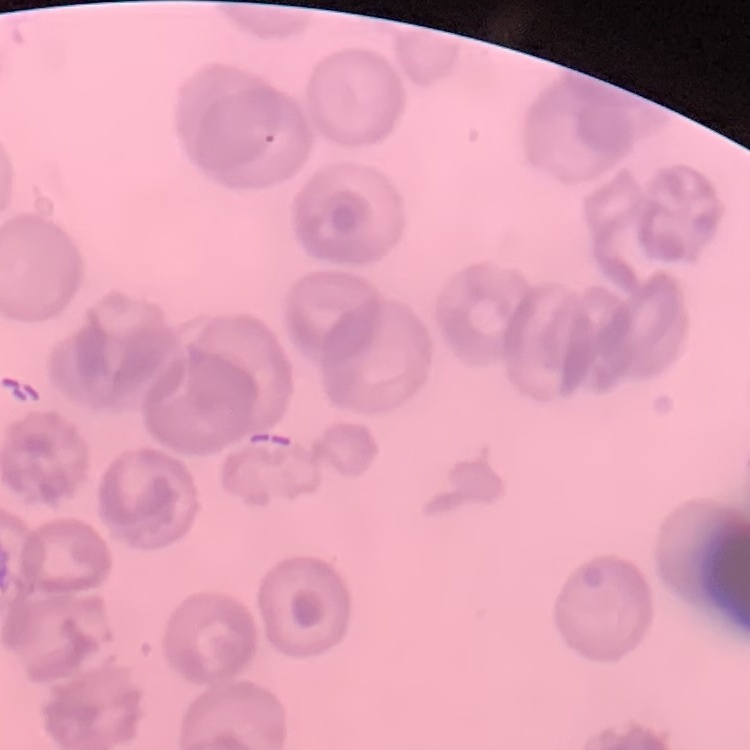

erythrocyte_morphology: no rouleaux formation
stain: Field's or Giemsa
image_type: one tile cut from a larger photomicrograph
preparation: thin blood smear